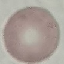
Result: negative for malaria parasites. Automatically extracted cell patch, resized to 64 × 64 pixels. Thin blood film. Giemsa stain. Acquired by smartphone through the microscope eyepiece.